Assess this cell for malaria.
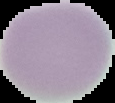
It is uninfected.

Image is 115×103 pixels. Segmented cell region on a black background. From a thin blood smear.